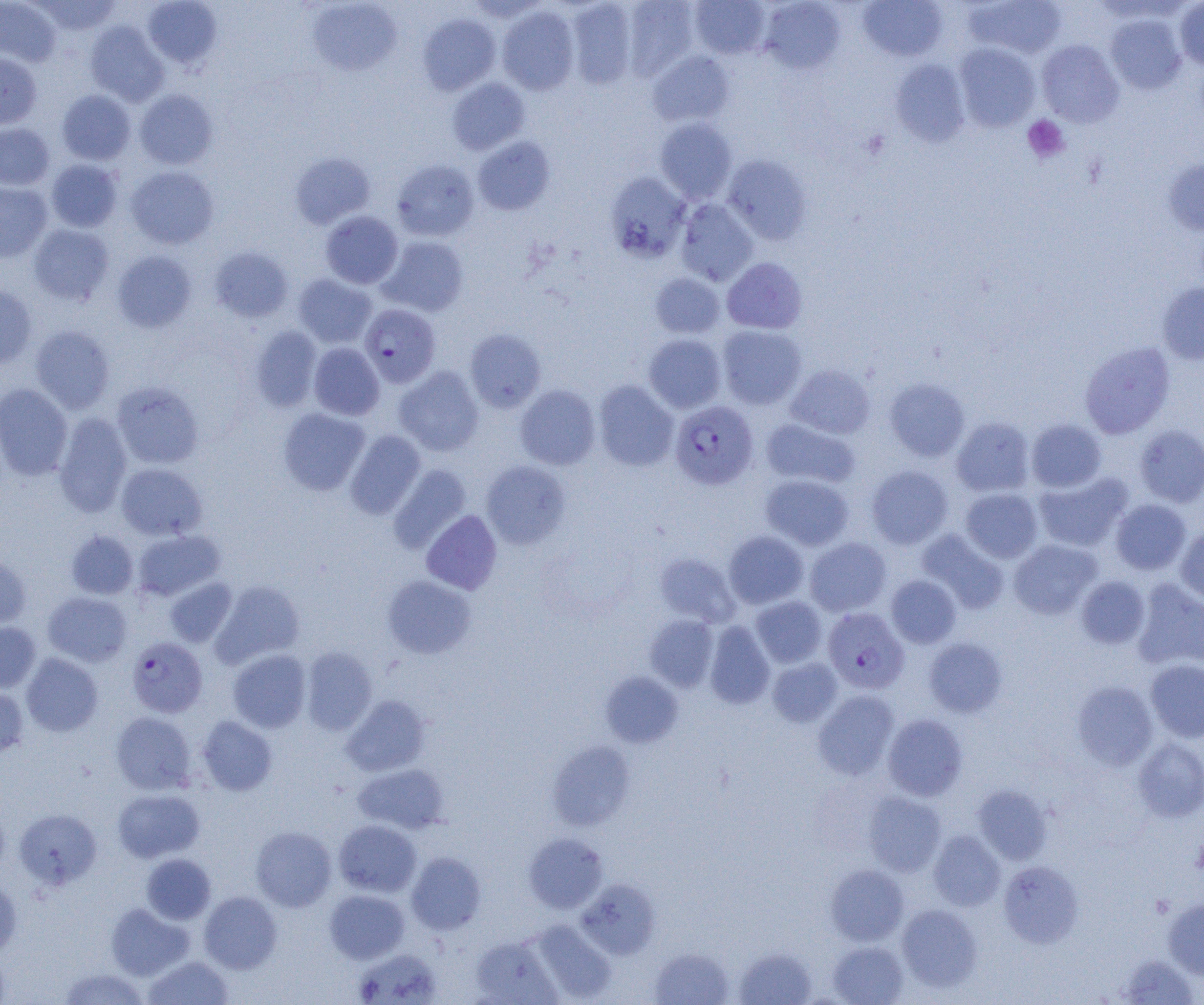
slide-level diagnosis = Plasmodium falciparum
preparation = thin blood smear
Plasmodium falciparum-infected red blood cell locations = approximate bounding boxes as [x1, y1, x2, y2] in pixels: [359, 303, 441, 387], [670, 401, 758, 489], [823, 607, 909, 694], [126, 637, 207, 718]
field of view = one of a larger specimen
platelet locations = approximate bounding boxes as [x1, y1, x2, y2] in pixels: [1022, 115, 1070, 164], [1192, 836, 1204, 877]
modality = light microscopy
magnification = 1000x
image size = 1204×1005 pixels
uninfected red blood cell locations = approximate bounding boxes as [x1, y1, x2, y2] in pixels: [0, 0, 61, 67], [34, 0, 122, 36], [143, 0, 222, 68], [621, 0, 700, 81], [858, 0, 948, 61], [962, 0, 1067, 59], [307, 1, 401, 76], [565, 1, 637, 90], [690, 1, 770, 59], [758, 1, 844, 73], [1175, 1, 1204, 71], [497, 6, 580, 95], [417, 13, 501, 95], [1105, 13, 1187, 94], [85, 21, 168, 106], [1036, 39, 1124, 127], [954, 43, 1041, 131], [647, 51, 735, 127], [0, 53, 42, 129], [890, 59, 971, 147], [447, 78, 530, 155], [135, 89, 218, 170], [57, 90, 136, 165], [654, 118, 737, 203], [0, 123, 54, 190], [473, 136, 555, 215], [290, 152, 375, 229], [723, 154, 812, 244], [1163, 158, 1204, 236], [391, 159, 478, 242], [46, 160, 122, 232], [126, 166, 219, 249], [605, 172, 691, 263], [0, 182, 52, 262], [675, 198, 758, 286], [320, 211, 403, 289], [28, 224, 113, 305], [379, 236, 469, 317], [210, 246, 293, 322], [112, 251, 196, 333], [722, 257, 807, 334], [650, 273, 725, 339], [293, 274, 377, 348], [1157, 282, 1204, 365], [0, 284, 37, 368], [30, 325, 115, 414], [717, 325, 807, 409], [250, 326, 322, 411], [465, 329, 546, 412], [643, 333, 726, 413], [1079, 341, 1175, 438], [309, 343, 384, 420], [786, 364, 875, 439], [394, 366, 484, 456], [884, 378, 970, 461], [593, 380, 679, 471], [111, 381, 204, 470], [0, 383, 73, 480], [515, 385, 600, 470], [278, 408, 370, 495], [53, 413, 133, 517], [951, 417, 1035, 497], [761, 418, 860, 489], [1026, 419, 1106, 492], [1135, 424, 1204, 507], [345, 430, 425, 519], [481, 461, 570, 549], [116, 463, 207, 540], [388, 464, 472, 554], [867, 465, 953, 549], [1034, 472, 1133, 552], [761, 474, 853, 550], [960, 488, 1042, 563], [1110, 499, 1191, 575], [422, 510, 502, 594], [1176, 527, 1204, 603], [133, 529, 225, 601], [917, 529, 1008, 614], [65, 530, 139, 599], [723, 530, 809, 609], [805, 537, 891, 616], [1009, 539, 1102, 619], [655, 552, 740, 626], [0, 554, 31, 628], [382, 575, 476, 659], [886, 575, 961, 648], [1076, 576, 1150, 649], [164, 577, 237, 647], [210, 580, 305, 668], [1132, 580, 1204, 671], [43, 592, 132, 667], [751, 596, 827, 668], [644, 615, 719, 692], [0, 621, 41, 692], [704, 621, 775, 709], [923, 637, 1007, 718], [301, 647, 377, 735], [228, 649, 311, 733], [21, 653, 103, 737], [767, 657, 842, 727], [1145, 660, 1204, 742], [601, 671, 683, 748], [1072, 681, 1158, 770], [0, 685, 29, 756], [813, 690, 900, 779], [341, 695, 430, 776], [111, 711, 196, 794], [883, 714, 968, 801], [197, 716, 278, 796], [1133, 738, 1204, 821], [547, 740, 636, 832], [353, 764, 448, 834], [973, 784, 1052, 865], [112, 789, 205, 863], [864, 792, 946, 876], [14, 808, 101, 889], [333, 820, 421, 897], [251, 826, 337, 911], [928, 830, 1005, 911], [523, 833, 607, 913], [406, 852, 486, 934], [141, 854, 216, 924], [999, 861, 1083, 947], [826, 864, 908, 945], [0, 878, 22, 960], [576, 878, 660, 959], [325, 889, 410, 963], [199, 891, 282, 973], [1163, 898, 1204, 979], [106, 903, 194, 980], [896, 904, 982, 991], [528, 920, 617, 1003], [470, 935, 562, 1005], [828, 941, 909, 1005], [734, 946, 817, 1005], [649, 947, 733, 1005], [353, 948, 443, 1004], [0, 950, 11, 1004], [143, 955, 234, 1004], [1116, 955, 1200, 1004], [58, 968, 149, 1004]